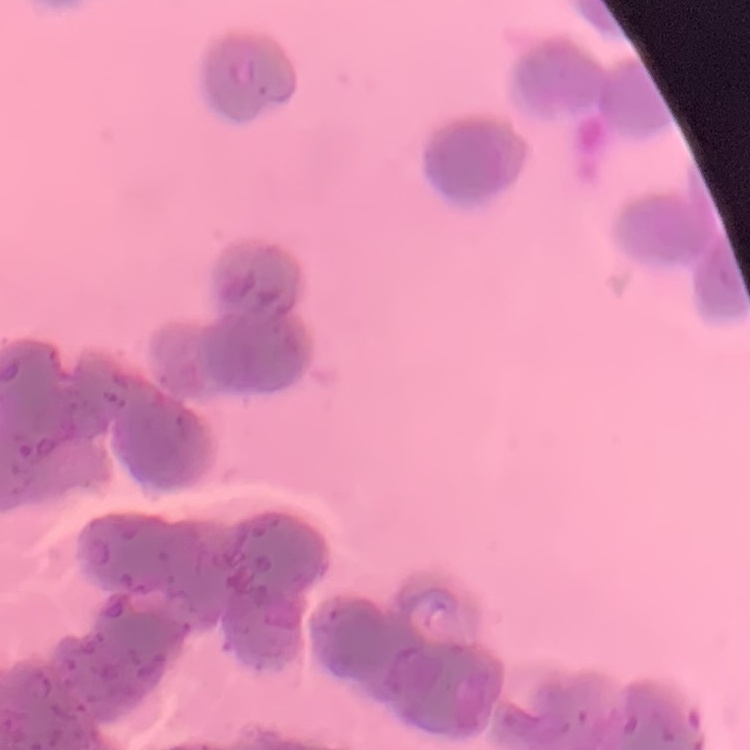
Summary:
  - Erythrocyte morphology: rouleaux formation
  - Stain: Field's or Giemsa
  - Preparation: thin blood smear
  - Image type: one tile cut from a larger photomicrograph